Report the malaria status of this cell.
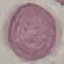

It is uninfected.

Summary:
  - Preparation: thin blood smear
  - Image type: automatically extracted cell patch, resized to 64 × 64 pixels
  - Stain: Giemsa
  - Capture: smartphone camera at the microscope eyepiece